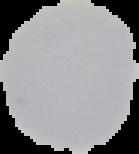

{
  "preparation": "thin blood film",
  "malaria_status": "uninfected",
  "image_size": "139×154 pixels",
  "image_type": "cell region segmented out of the field of view; surrounding area masked to black"
}